State the blood parasite species.
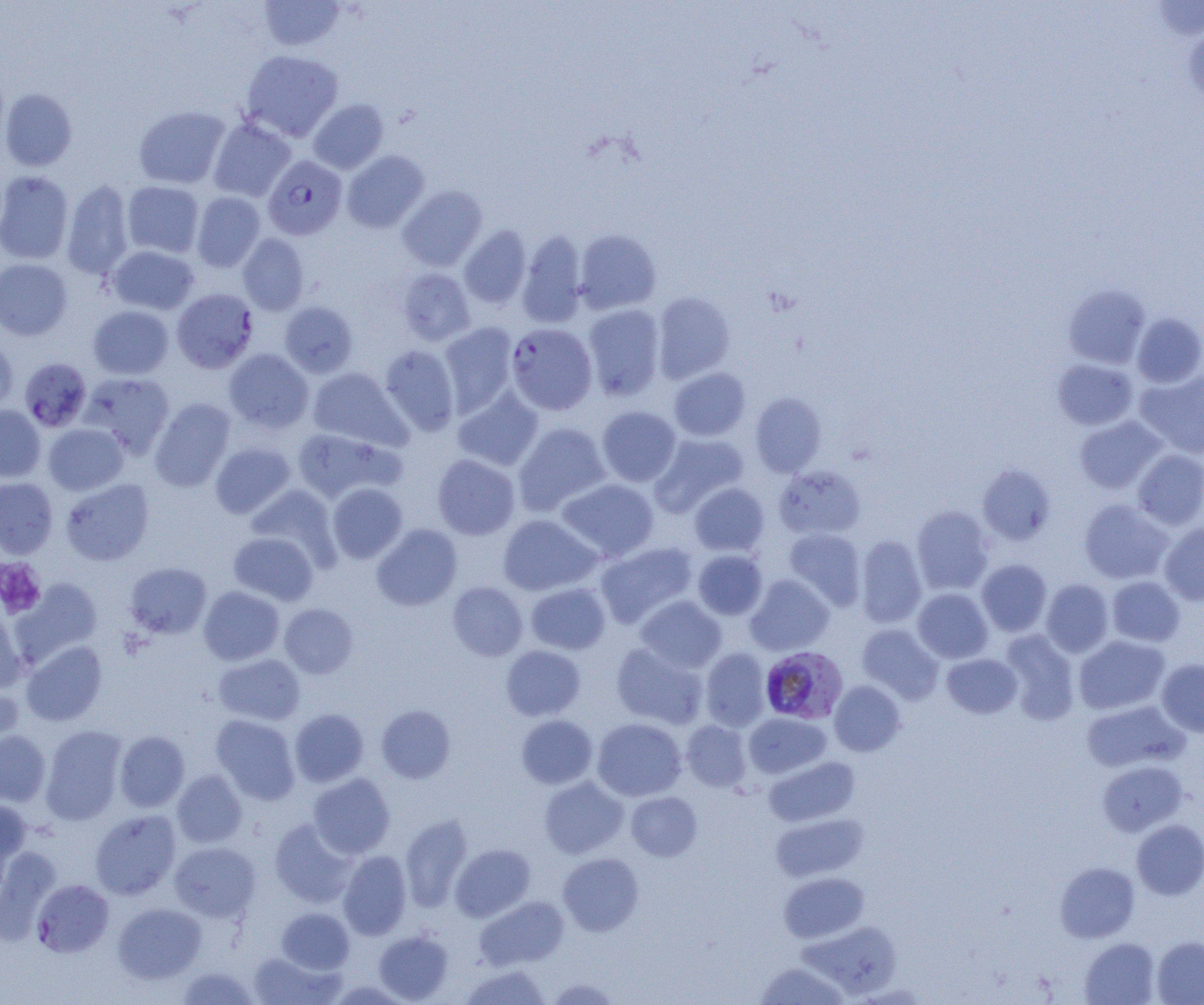

Plasmodium falciparum.

Approximate bounding boxes as named x1/y1/x2/y2 corners in pixels. Uninfected red blood cell locations (subset): (x1=258, y1=0, x2=346, y2=51), (x1=1149, y1=1, x2=1204, y2=42), (x1=1183, y1=21, x2=1204, y2=107), (x1=240, y1=49, x2=343, y2=142), (x1=1, y1=89, x2=78, y2=171), (x1=308, y1=98, x2=388, y2=174), (x1=133, y1=105, x2=230, y2=189), (x1=208, y1=117, x2=296, y2=202), (x1=341, y1=150, x2=430, y2=233), (x1=0, y1=170, x2=74, y2=264), (x1=61, y1=179, x2=134, y2=280), (x1=122, y1=181, x2=204, y2=258), (x1=397, y1=185, x2=488, y2=271), (x1=191, y1=192, x2=265, y2=272), (x1=459, y1=225, x2=531, y2=309), (x1=574, y1=229, x2=661, y2=314), (x1=517, y1=230, x2=587, y2=328), (x1=237, y1=233, x2=309, y2=315), (x1=107, y1=245, x2=199, y2=315), (x1=0, y1=258, x2=72, y2=340), (x1=396, y1=268, x2=475, y2=346), (x1=1063, y1=285, x2=1151, y2=368), (x1=652, y1=291, x2=735, y2=383), (x1=280, y1=301, x2=358, y2=378), (x1=582, y1=304, x2=665, y2=400), (x1=88, y1=305, x2=174, y2=379), (x1=1132, y1=313, x2=1204, y2=388), (x1=439, y1=322, x2=518, y2=416), (x1=0, y1=337, x2=17, y2=416), (x1=379, y1=345, x2=460, y2=436), (x1=224, y1=348, x2=313, y2=434), (x1=1052, y1=358, x2=1139, y2=430), (x1=307, y1=367, x2=410, y2=451), (x1=669, y1=367, x2=750, y2=441), (x1=1135, y1=370, x2=1204, y2=459), (x1=80, y1=372, x2=175, y2=459), (x1=453, y1=387, x2=544, y2=471), (x1=750, y1=392, x2=827, y2=477), (x1=150, y1=398, x2=235, y2=492), (x1=0, y1=405, x2=45, y2=481), (x1=597, y1=406, x2=681, y2=487), (x1=1074, y1=416, x2=1166, y2=494), (x1=514, y1=422, x2=611, y2=516), (x1=43, y1=423, x2=128, y2=495), (x1=291, y1=428, x2=398, y2=504), (x1=650, y1=433, x2=749, y2=516), (x1=210, y1=442, x2=295, y2=519), (x1=1133, y1=449, x2=1204, y2=530), (x1=432, y1=454, x2=520, y2=540), (x1=978, y1=464, x2=1055, y2=545), (x1=775, y1=465, x2=865, y2=540), (x1=0, y1=478, x2=58, y2=559), (x1=557, y1=478, x2=658, y2=561), (x1=61, y1=479, x2=154, y2=566), (x1=689, y1=482, x2=769, y2=556), (x1=327, y1=483, x2=408, y2=563), (x1=245, y1=484, x2=339, y2=567), (x1=1079, y1=498, x2=1173, y2=584), (x1=911, y1=506, x2=994, y2=595), (x1=498, y1=514, x2=601, y2=595), (x1=1159, y1=522, x2=1204, y2=606), (x1=372, y1=524, x2=462, y2=611), (x1=784, y1=529, x2=866, y2=610), (x1=229, y1=531, x2=319, y2=606), (x1=856, y1=534, x2=926, y2=628), (x1=595, y1=542, x2=698, y2=628), (x1=693, y1=550, x2=768, y2=620), (x1=977, y1=559, x2=1052, y2=636), (x1=125, y1=562, x2=212, y2=639), (x1=745, y1=574, x2=834, y2=655), (x1=1107, y1=576, x2=1185, y2=647), (x1=12, y1=577, x2=103, y2=665), (x1=1041, y1=578, x2=1114, y2=657), (x1=447, y1=582, x2=528, y2=661), (x1=526, y1=582, x2=610, y2=654), (x1=199, y1=586, x2=284, y2=665), (x1=913, y1=588, x2=993, y2=663), (x1=635, y1=595, x2=726, y2=673), (x1=0, y1=601, x2=27, y2=692), (x1=279, y1=603, x2=358, y2=679), (x1=857, y1=623, x2=944, y2=704), (x1=999, y1=630, x2=1080, y2=723), (x1=1074, y1=635, x2=1170, y2=714), (x1=21, y1=640, x2=107, y2=726), (x1=611, y1=642, x2=707, y2=729), (x1=501, y1=645, x2=586, y2=721), (x1=700, y1=648, x2=771, y2=731), (x1=942, y1=653, x2=1022, y2=719), (x1=214, y1=654, x2=305, y2=726), (x1=1156, y1=659, x2=1204, y2=737), (x1=0, y1=681, x2=23, y2=755), (x1=829, y1=681, x2=906, y2=756), (x1=1081, y1=700, x2=1188, y2=773), (x1=376, y1=705, x2=456, y2=783), (x1=289, y1=709, x2=368, y2=787), (x1=743, y1=712, x2=831, y2=779), (x1=211, y1=714, x2=300, y2=805), (x1=515, y1=715, x2=598, y2=789), (x1=592, y1=718, x2=686, y2=801), (x1=681, y1=720, x2=752, y2=792), (x1=40, y1=726, x2=127, y2=825), (x1=0, y1=730, x2=50, y2=806), (x1=114, y1=731, x2=189, y2=812), (x1=764, y1=756, x2=859, y2=827), (x1=1097, y1=760, x2=1187, y2=836), (x1=172, y1=769, x2=248, y2=848), (x1=308, y1=773, x2=395, y2=859), (x1=539, y1=777, x2=628, y2=858), (x1=626, y1=792, x2=702, y2=861), (x1=0, y1=799, x2=31, y2=880), (x1=90, y1=810, x2=181, y2=900), (x1=770, y1=812, x2=868, y2=882), (x1=400, y1=814, x2=473, y2=911), (x1=269, y1=819, x2=357, y2=907), (x1=1132, y1=819, x2=1204, y2=899), (x1=169, y1=841, x2=261, y2=922), (x1=450, y1=843, x2=535, y2=922), (x1=0, y1=849, x2=61, y2=941), (x1=338, y1=850, x2=412, y2=940), (x1=558, y1=853, x2=644, y2=936), (x1=1055, y1=862, x2=1140, y2=942), (x1=779, y1=872, x2=868, y2=943), (x1=474, y1=895, x2=568, y2=970), (x1=113, y1=903, x2=206, y2=984), (x1=277, y1=907, x2=354, y2=974), (x1=799, y1=920, x2=902, y2=998), (x1=373, y1=929, x2=453, y2=1003), (x1=1152, y1=936, x2=1204, y2=1005), (x1=1080, y1=937, x2=1160, y2=1005), (x1=248, y1=950, x2=342, y2=1005), (x1=754, y1=961, x2=851, y2=1004), (x1=459, y1=964, x2=551, y2=1005), (x1=176, y1=966, x2=259, y2=1004), (x1=546, y1=978, x2=622, y2=1004). Platelet locations: (x1=0, y1=558, x2=46, y2=618). Plasmodium falciparum-infected red blood cell locations (subset): (x1=263, y1=155, x2=347, y2=240), (x1=506, y1=323, x2=597, y2=415), (x1=20, y1=359, x2=93, y2=434), (x1=760, y1=646, x2=848, y2=723), (x1=31, y1=879, x2=114, y2=957). Light microscopy. Image is 1204×1005 pixels. Thin blood smear. 1000x magnification. One field of a larger specimen.